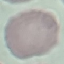
Summary:
  - Result: no malaria parasites detected
  - Stain: Giemsa
  - Capture: smartphone through the microscope eyepiece
  - Preparation: thin blood film
  - Image type: cell patch, automatically extracted from a larger field of view and resized to 64 × 64 pixels